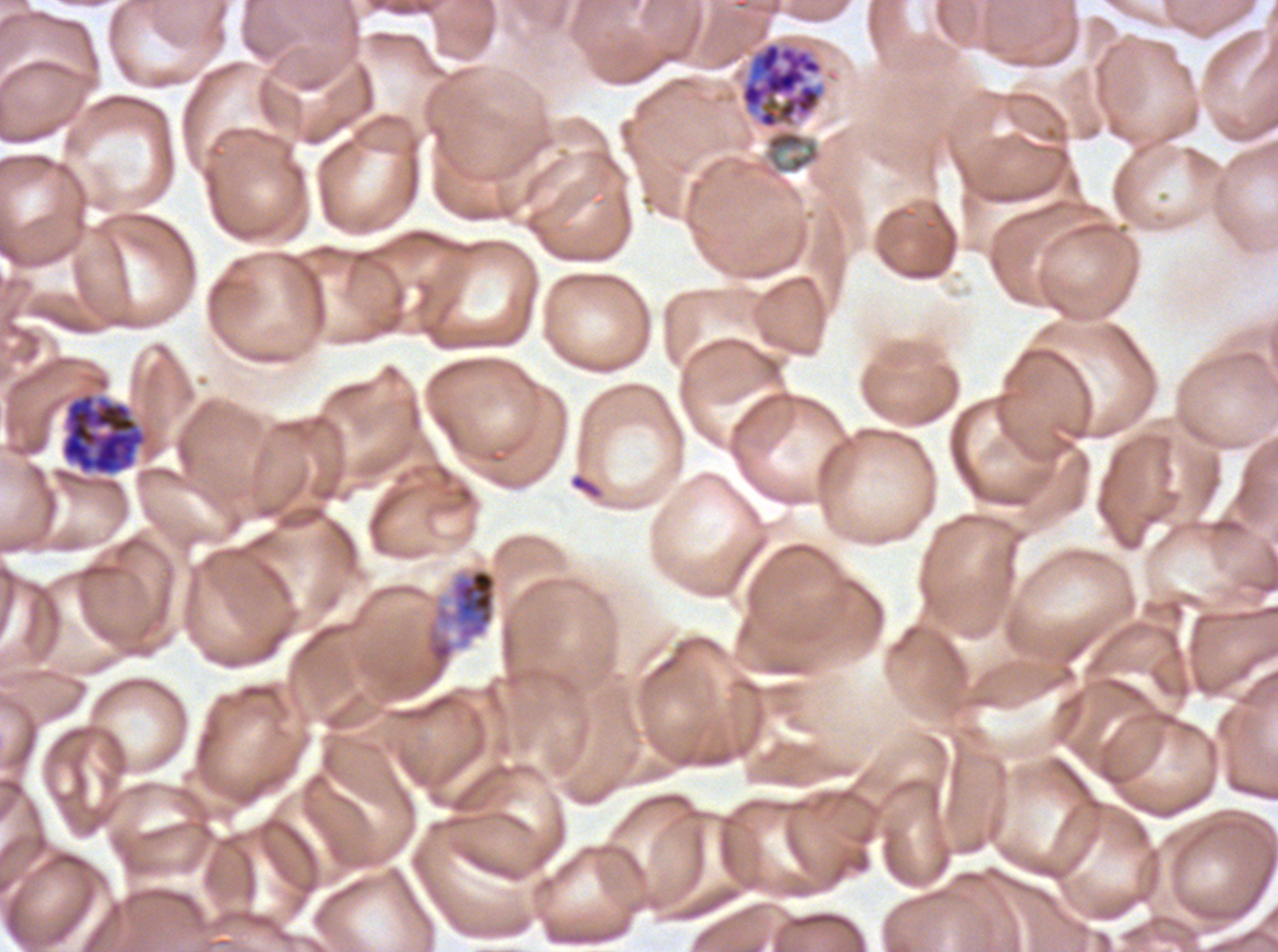

Approximate bounding boxes as (x1, y1, x2, y2) in pixels.
Summary:
  - Late schizont locations: (738, 40, 828, 130)
  - Early schizont locations: (61, 393, 146, 475), (434, 567, 498, 646)
  - Image size: 1278×952 pixels
  - Life-cycle stages observed: early schizont, late schizont
  - Preparation: thin blood film
  - Stain: Giemsa
  - Field of view: sub-image separated from a larger composite
  - Specimen: P. falciparum from a patient in The Gambia, cultured ex vivo for 24 to 48 hours